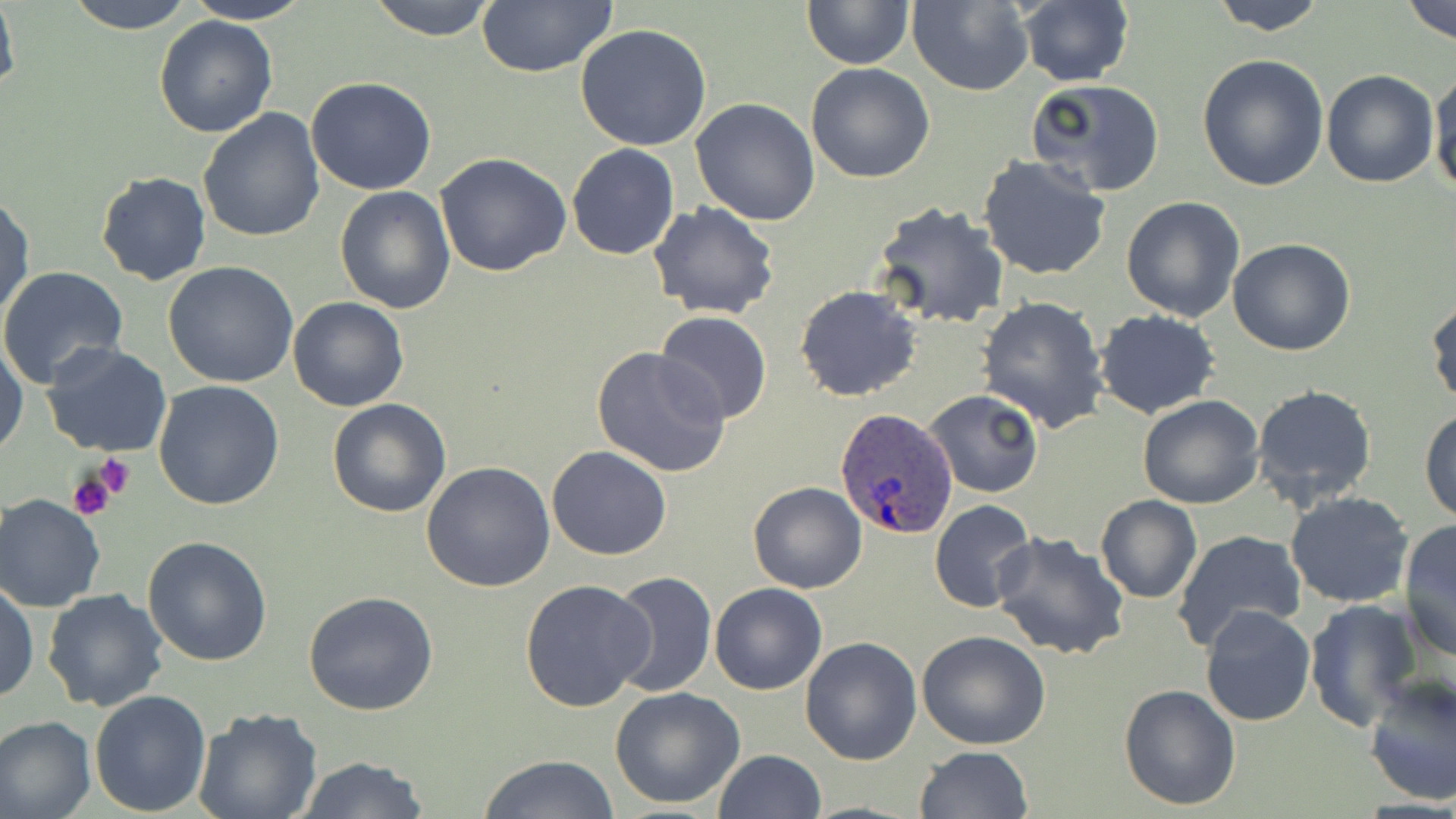 Approximate bounding boxes as (x1, y1, x2, y2) in pixels. Uninfected red blood cell locations: (0, 0, 21, 102), (64, 0, 198, 33), (181, 0, 316, 24), (366, 0, 500, 39), (801, 0, 913, 69), (1208, 0, 1330, 34), (1402, 0, 1456, 43), (475, 1, 620, 77), (907, 1, 1034, 94), (1015, 1, 1134, 87), (152, 14, 278, 138), (574, 24, 713, 151), (1196, 54, 1329, 193), (806, 62, 935, 183), (1429, 69, 1456, 197), (1320, 70, 1439, 187), (306, 77, 436, 195), (1027, 78, 1166, 197), (690, 98, 823, 226), (198, 108, 325, 246), (567, 143, 680, 260), (434, 153, 572, 277), (977, 156, 1113, 280), (95, 172, 213, 286), (335, 186, 456, 314), (0, 191, 35, 325), (1121, 195, 1247, 322), (647, 200, 780, 319), (870, 201, 1009, 332), (1228, 238, 1355, 357), (165, 262, 300, 388), (0, 266, 130, 387), (795, 285, 922, 401), (1426, 292, 1456, 408), (287, 295, 409, 413), (976, 295, 1109, 434), (1093, 309, 1221, 420), (654, 311, 774, 426), (0, 337, 27, 460), (40, 340, 174, 458), (589, 346, 733, 480), (153, 380, 286, 510), (1251, 382, 1380, 511), (925, 389, 1044, 497), (1137, 394, 1266, 509), (327, 398, 451, 518), (1419, 407, 1456, 525), (547, 446, 672, 561), (421, 461, 555, 592), (748, 482, 866, 593), (1284, 490, 1415, 609), (0, 495, 105, 612), (1095, 495, 1203, 604), (929, 501, 1038, 613), (1398, 518, 1456, 662), (1172, 529, 1306, 650), (990, 530, 1130, 661), (142, 535, 276, 667), (608, 571, 717, 698), (518, 578, 655, 712), (1, 581, 38, 704), (709, 583, 828, 695), (41, 589, 170, 713), (303, 592, 438, 715), (1303, 599, 1422, 729), (1200, 604, 1316, 727), (917, 630, 1051, 750), (799, 636, 922, 765), (1361, 673, 1456, 807), (1118, 683, 1240, 811), (610, 685, 746, 809), (89, 689, 212, 814), (193, 708, 324, 819), (0, 715, 97, 819), (916, 746, 1034, 819), (712, 749, 826, 819), (478, 754, 619, 819), (294, 756, 430, 819). Platelet locations: (95, 456, 136, 499), (66, 468, 120, 523). Plasmodium ovale-infected red blood cell locations: (833, 407, 959, 540). Slide-level diagnosis: Plasmodium ovale. Thin blood film. One field of a larger specimen. Light microscopy. May-Grünwald-Giemsa-stained preparation. Image is 1456×819 pixels. Captured at 1000x magnification.